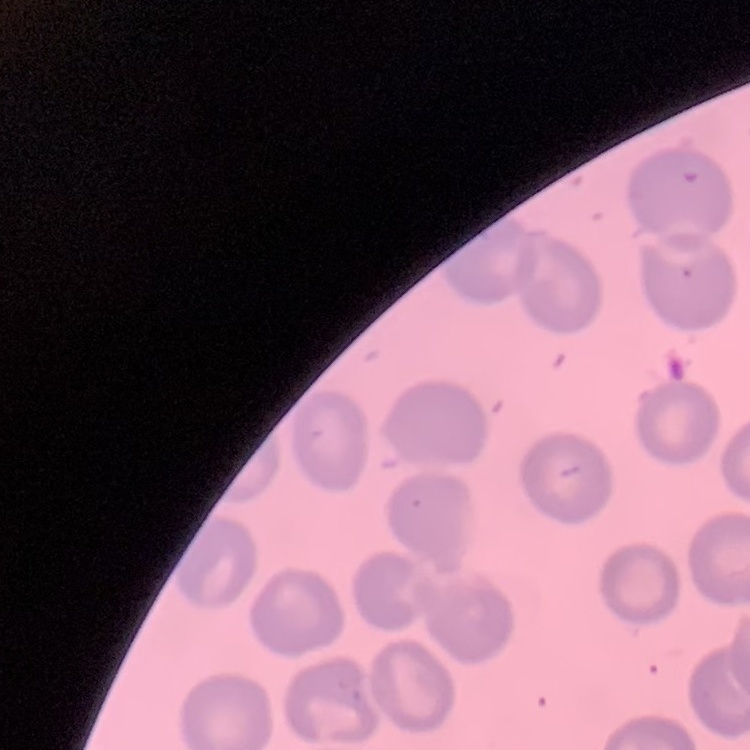
red blood cell morphology = no rouleaux formation
preparation = thin blood smear
stain = Field's or Giemsa
image type = one tile cut from a larger photomicrograph